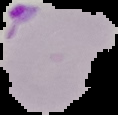
Result: Plasmodium parasites detected. Image is 118×115 pixels. From a thin blood smear. Cell region segmented out of the field of view; the surrounding area is masked to black.